Locate and identify every blood parasite.
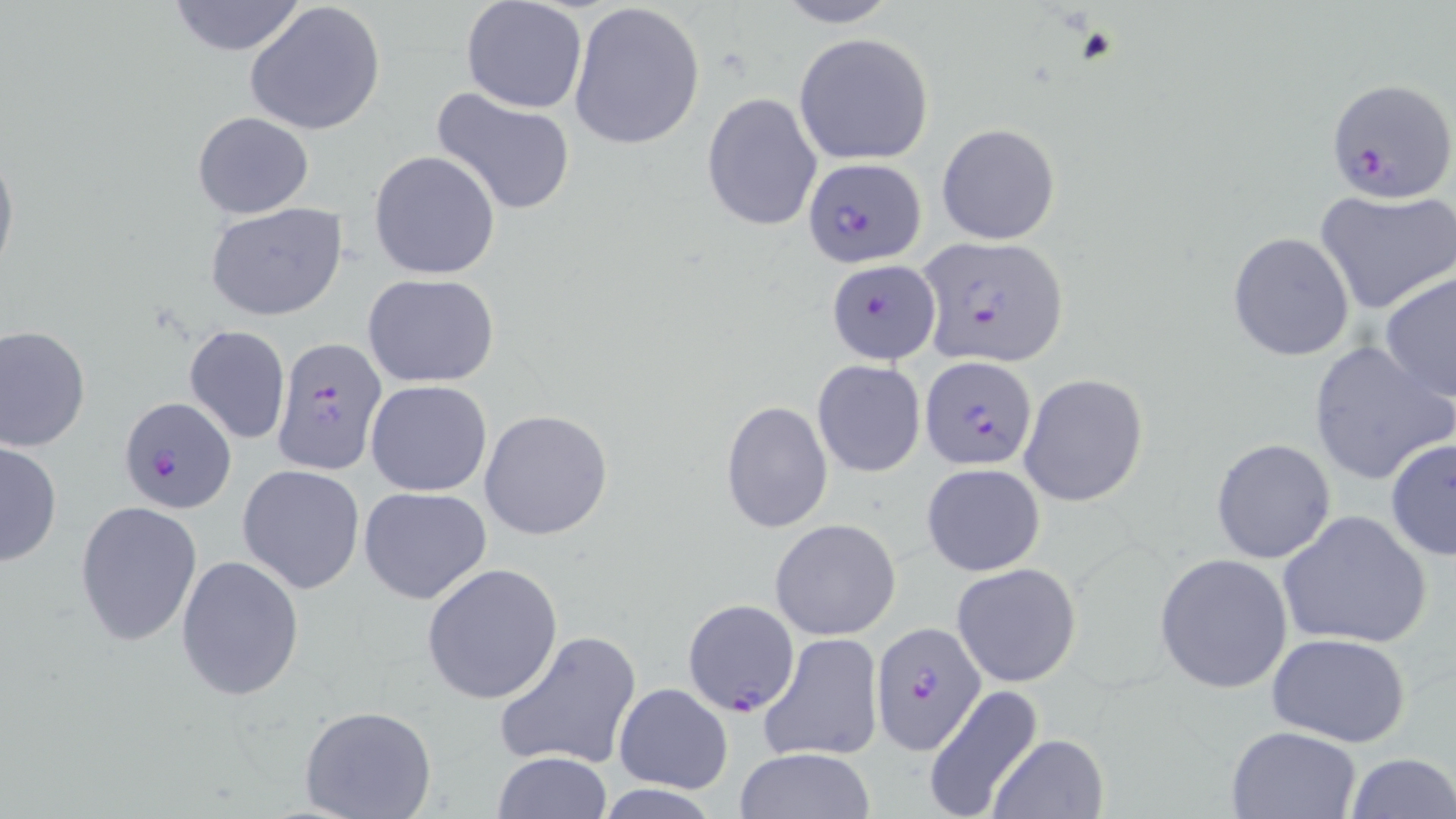
Approximate bounding boxes as [x1, y1, x2, y2] in pixels.
Plasmodium falciparum-infected red blood cells: [1325, 77, 1456, 204], [803, 156, 927, 268], [922, 237, 1070, 366], [826, 259, 940, 363], [270, 334, 389, 475], [919, 357, 1037, 470], [116, 396, 235, 513], [683, 601, 801, 716], [873, 623, 987, 756].
No Plasmodium ovale, Plasmodium malariae, Plasmodium vivax, Babesia divergens, or Trypanosoma brucei observed.

Uninfected red blood cell locations: [163, 0, 312, 56], [769, 0, 902, 28], [243, 1, 387, 136], [460, 2, 587, 114], [567, 2, 707, 151], [793, 33, 934, 165], [430, 85, 579, 218], [700, 92, 823, 232], [191, 112, 316, 221], [936, 123, 1061, 245], [0, 138, 19, 286], [368, 149, 501, 280], [1315, 189, 1456, 316], [205, 202, 349, 321], [1227, 232, 1356, 360], [1380, 270, 1456, 403], [362, 273, 499, 388], [0, 323, 90, 452], [183, 325, 291, 445], [1306, 340, 1455, 488], [812, 359, 927, 478], [1020, 373, 1148, 506], [365, 379, 493, 497], [719, 400, 833, 534], [480, 409, 614, 542], [1384, 436, 1456, 561], [1211, 438, 1337, 564], [1, 440, 63, 569], [922, 462, 1045, 575], [237, 464, 365, 595], [359, 486, 492, 604], [74, 500, 203, 646], [1278, 509, 1433, 651], [770, 518, 902, 640], [1155, 552, 1294, 694], [176, 554, 305, 700], [420, 562, 563, 706], [951, 562, 1082, 687], [493, 628, 642, 771], [760, 631, 884, 763], [1265, 633, 1411, 747], [612, 682, 732, 793], [920, 685, 1044, 819], [299, 705, 438, 819], [1226, 726, 1361, 818], [988, 733, 1110, 818], [732, 748, 876, 819], [491, 751, 615, 819], [1343, 752, 1455, 819]. Slide-level diagnosis: Plasmodium falciparum. Light microscopy. Thin blood smear. May-Grünwald-Giemsa-stained preparation. Captured at 1000x magnification. Single field of view. Image is 1456×819 pixels.